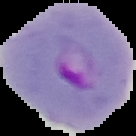

malaria status = parasitized
preparation = thin blood smear
image size = 136×136 pixels
image type = cell region segmented out of the field of view; surrounding area masked to black